State which parasite is depicted.
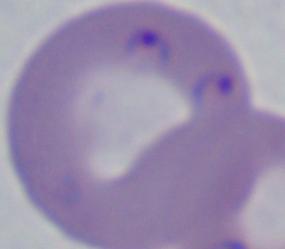
This is Babesia.

Summary:
  - Magnification: 1000x
  - Modality: photomicrograph